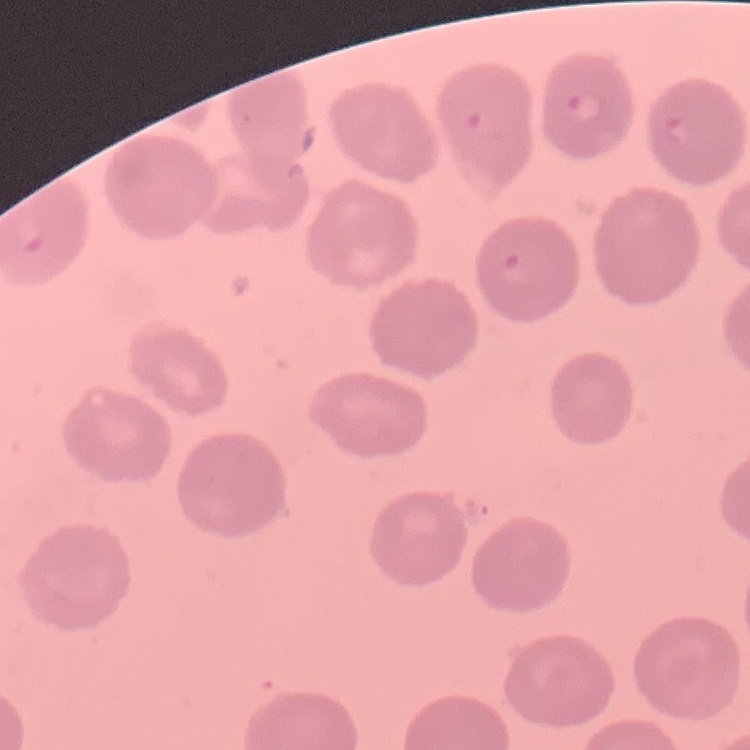

The erythrocytes exhibit no rouleaux formation. Stained with either Field's or Giemsa. Thin peripheral smear. One tile cut from a larger photomicrograph.